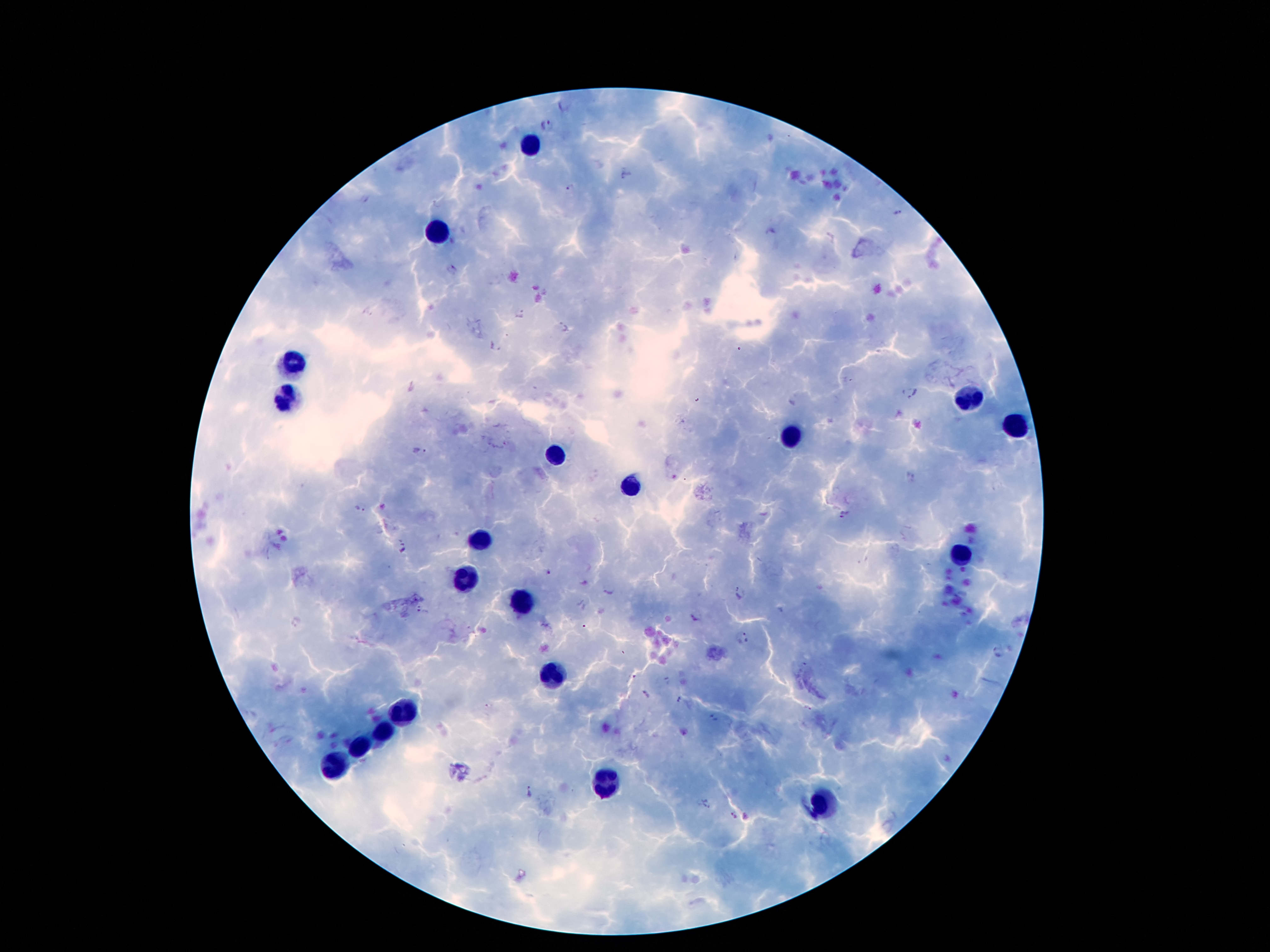

Approximate centers as [x, y] in pixels.
Summary:
  - Leukocyte locations: [529, 145], [434, 234], [295, 361], [286, 399], [970, 404], [1018, 426], [793, 435], [554, 452], [629, 487], [481, 542], [961, 556], [463, 581], [521, 604], [551, 678], [403, 711], [383, 732], [359, 746], [335, 766], [607, 782], [821, 802]
  - Malaria parasite locations: [549, 124], [570, 188], [365, 200], [451, 271], [368, 313], [521, 314], [561, 329], [494, 347], [909, 392], [419, 452], [359, 509], [846, 514], [405, 549], [549, 572], [740, 592], [423, 611], [692, 618], [749, 636], [998, 653], [646, 694], [679, 701], [489, 707], [712, 718], [529, 791], [708, 804], [738, 817]
  - Magnification: 100x
  - Patient malaria status: positive for Plasmodium falciparum
  - Stain: Giemsa
  - Field of view: single
  - Capture: smartphone camera through the microscope eyepiece
  - Image size: 1270×952 pixels
  - Preparation: thick peripheral-blood smear